Assess the morphology of the red blood cells.
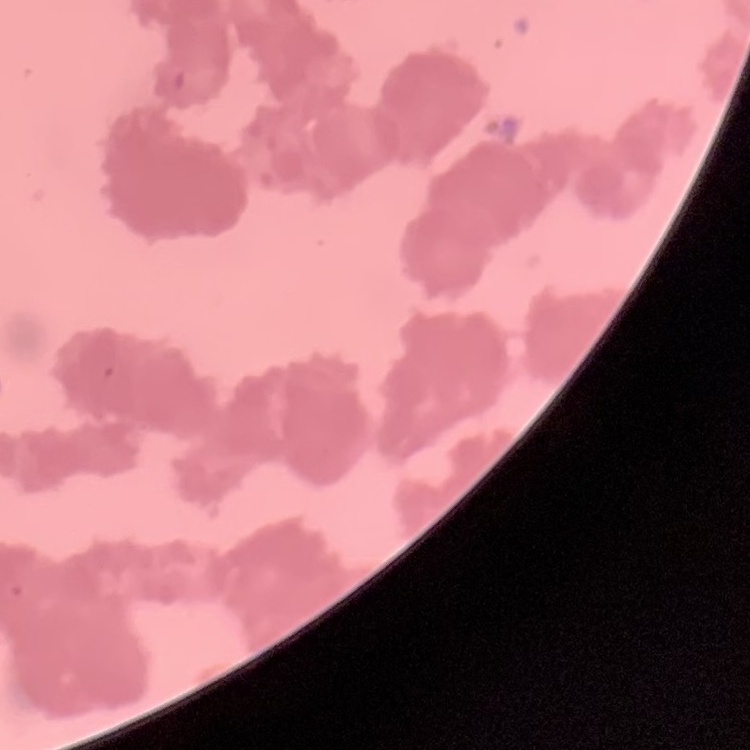

Rouleaux formation.

preparation = thin peripheral smear
image type = one tile cut from a larger photomicrograph
stain = Field's or Giemsa